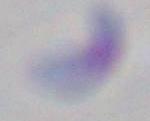

identification = Toxoplasma gondii
magnification = 1000x
modality = micrograph